Report the malaria status of this cell.
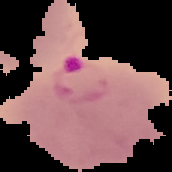
It is parasitized.

preparation: thin blood smear
image_type: cell region segmented out of the field of view; surrounding area masked to black
image_size: 172×172 pixels